Describe the morphology of the erythrocytes.
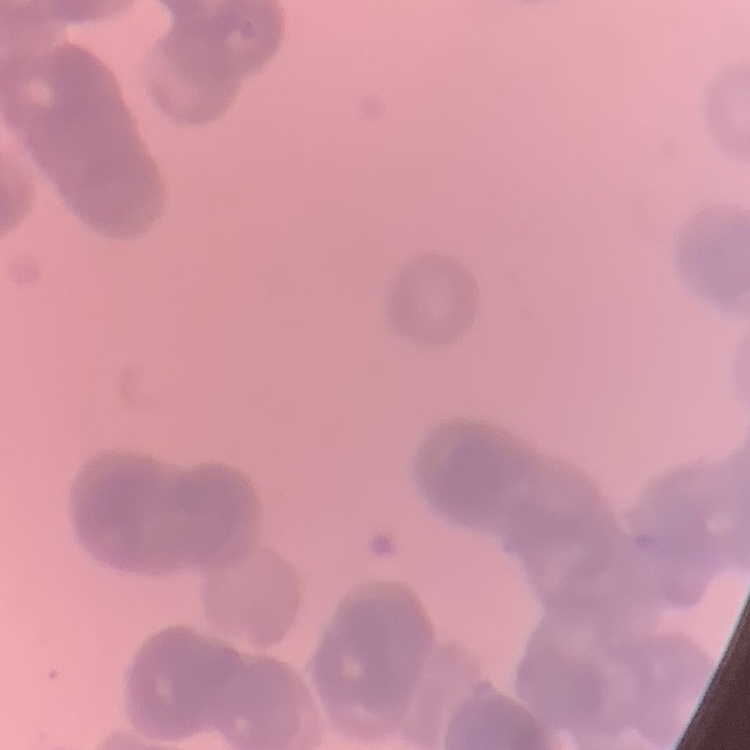
Rouleaux formation.

Thin peripheral smear. Field's or Giemsa stain. Square crop of a larger photomicrograph.